State which parasite is depicted.
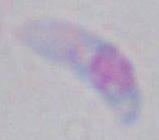
This is Toxoplasma gondii.

Captured at 1000x magnification. Photomicrograph.